Name the parasite shown.
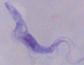

A trypanosome.

modality: photomicrograph
magnification: 1000x